Assess the morphology of the red blood cells.
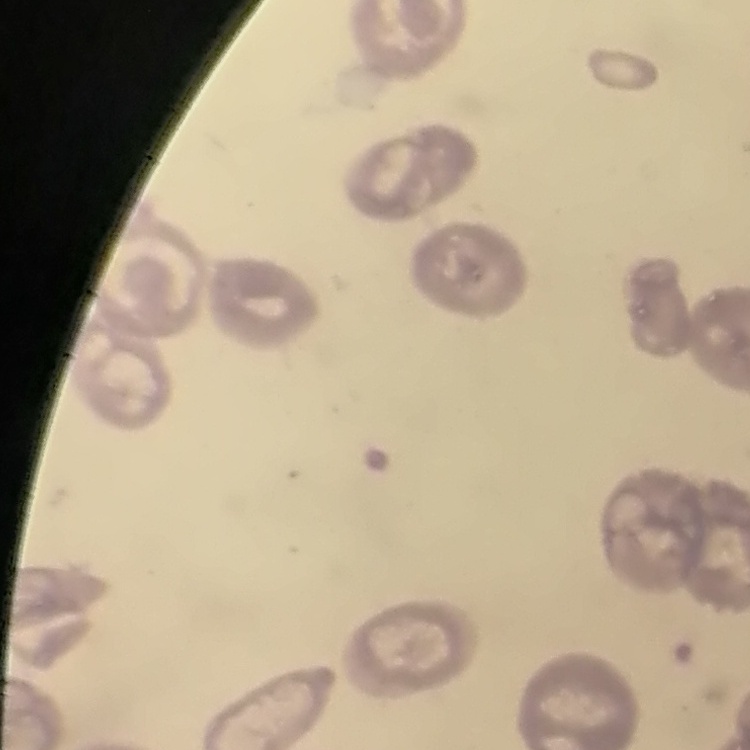

No rouleaux formation.

Summary:
  - Preparation: thin peripheral smear
  - Stain: Field's or Giemsa
  - Image type: square crop of a larger photomicrograph